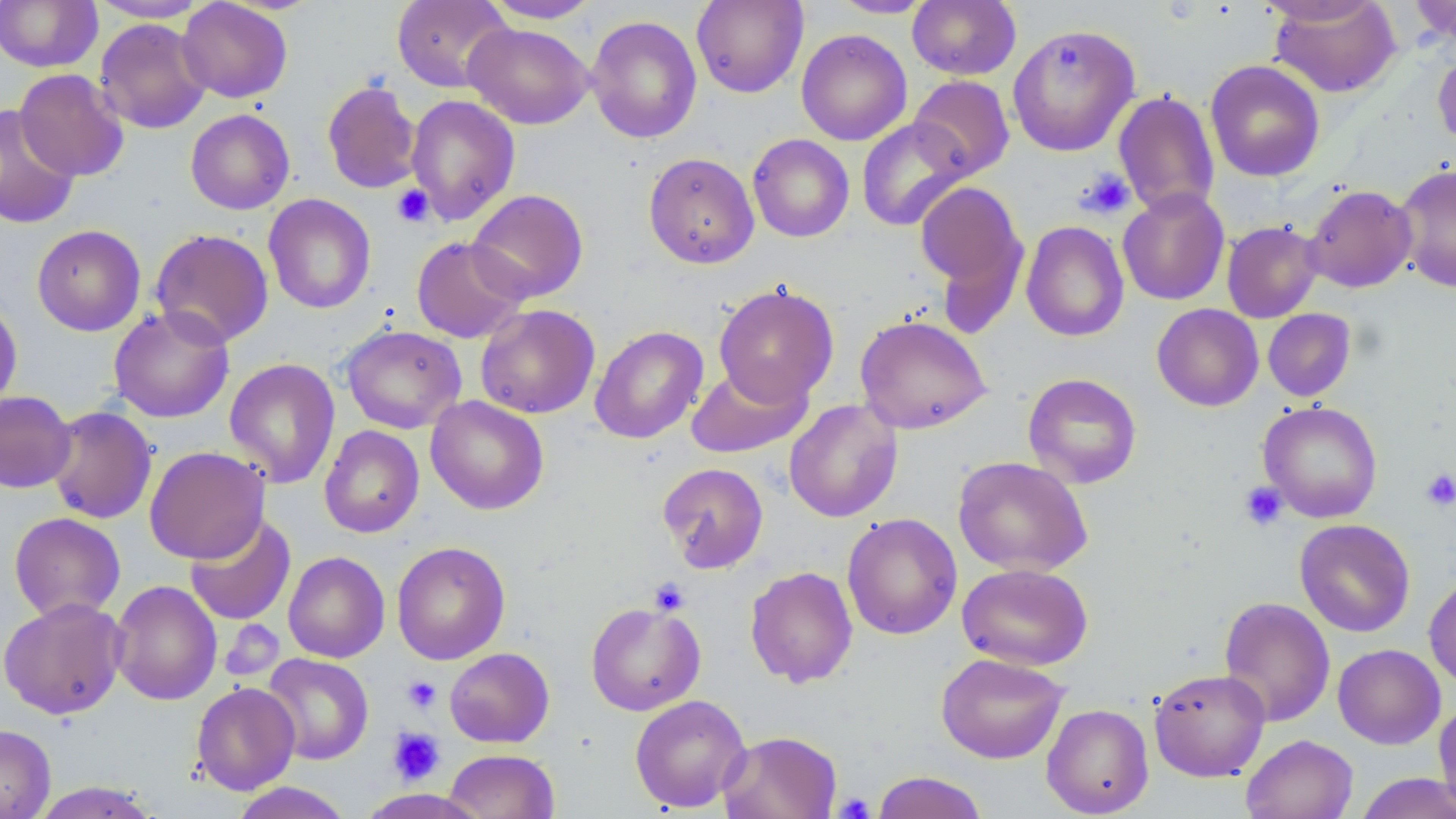
slide-level diagnosis = negative for blood parasites
modality = optical microscopy
platelet locations = approximate bounding boxes as (x1, y1, x2, y2) in pixels: (1077, 168, 1136, 219), (391, 184, 434, 228), (1420, 468, 1456, 512), (1239, 482, 1288, 532), (649, 578, 690, 616), (402, 675, 442, 713), (388, 727, 445, 785), (832, 792, 876, 819)
field of view = single
stain = May-Grünwald-Giemsa
magnification = 1000x
image size = 1456×819 pixels
preparation = thin blood smear
uninfected red blood cell locations = approximate bounding boxes as (x1, y1, x2, y2) in pixels: (0, 0, 102, 73), (88, 0, 210, 22), (176, 0, 293, 103), (483, 0, 601, 23), (691, 0, 808, 98), (828, 0, 935, 18), (907, 0, 1021, 80), (1256, 0, 1386, 26), (1269, 0, 1400, 97), (1409, 0, 1456, 46), (392, 1, 512, 92), (586, 15, 702, 144), (94, 18, 212, 134), (463, 22, 594, 129), (1007, 23, 1140, 157), (796, 29, 912, 145), (1432, 45, 1456, 154), (1205, 59, 1325, 182), (14, 69, 129, 181), (908, 75, 1015, 180), (322, 79, 422, 194), (1113, 89, 1220, 218), (405, 94, 521, 225), (0, 103, 80, 230), (185, 109, 295, 214), (856, 117, 971, 231), (748, 133, 854, 241), (643, 152, 759, 269), (1395, 164, 1456, 293), (914, 179, 1026, 310), (1303, 184, 1417, 293), (1118, 188, 1229, 305), (466, 189, 589, 303), (263, 194, 376, 314), (1222, 220, 1323, 323), (1021, 221, 1129, 342), (31, 225, 146, 336), (150, 228, 274, 348), (411, 236, 529, 343), (714, 283, 839, 407), (0, 300, 23, 414), (476, 304, 600, 419), (1152, 304, 1263, 411), (108, 305, 235, 423), (1262, 308, 1357, 401), (854, 315, 992, 434), (340, 325, 466, 433), (589, 325, 708, 444), (224, 358, 341, 489), (686, 363, 811, 458), (1023, 373, 1142, 489), (0, 390, 76, 493), (425, 396, 549, 515), (784, 399, 902, 523), (1258, 401, 1383, 523), (45, 405, 158, 524), (319, 425, 425, 538), (144, 446, 270, 564), (953, 455, 1092, 576), (657, 462, 769, 573), (9, 512, 126, 622), (842, 512, 962, 640), (184, 513, 296, 626), (1294, 519, 1415, 637), (391, 541, 511, 664), (283, 551, 390, 663), (957, 562, 1093, 671), (745, 566, 858, 688), (1424, 574, 1456, 688), (109, 579, 222, 706), (1218, 596, 1336, 727), (0, 597, 127, 720), (585, 601, 706, 716), (1333, 644, 1445, 749), (444, 647, 554, 747), (936, 652, 1069, 764), (261, 653, 374, 765), (1149, 667, 1270, 781), (190, 681, 300, 795), (630, 694, 751, 813), (1434, 701, 1456, 815), (1041, 703, 1154, 817), (0, 724, 55, 819), (718, 731, 842, 819), (1241, 734, 1358, 819), (443, 749, 559, 819), (871, 771, 989, 819), (1355, 772, 1456, 819), (29, 782, 163, 818), (229, 782, 354, 819)